Assess this cell for malaria.
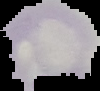

Parasitized.

Image is 100×91 pixels. From a thin blood film. Cell region segmented out of the field of view; the surrounding area is masked to black.